State the blood parasite species.
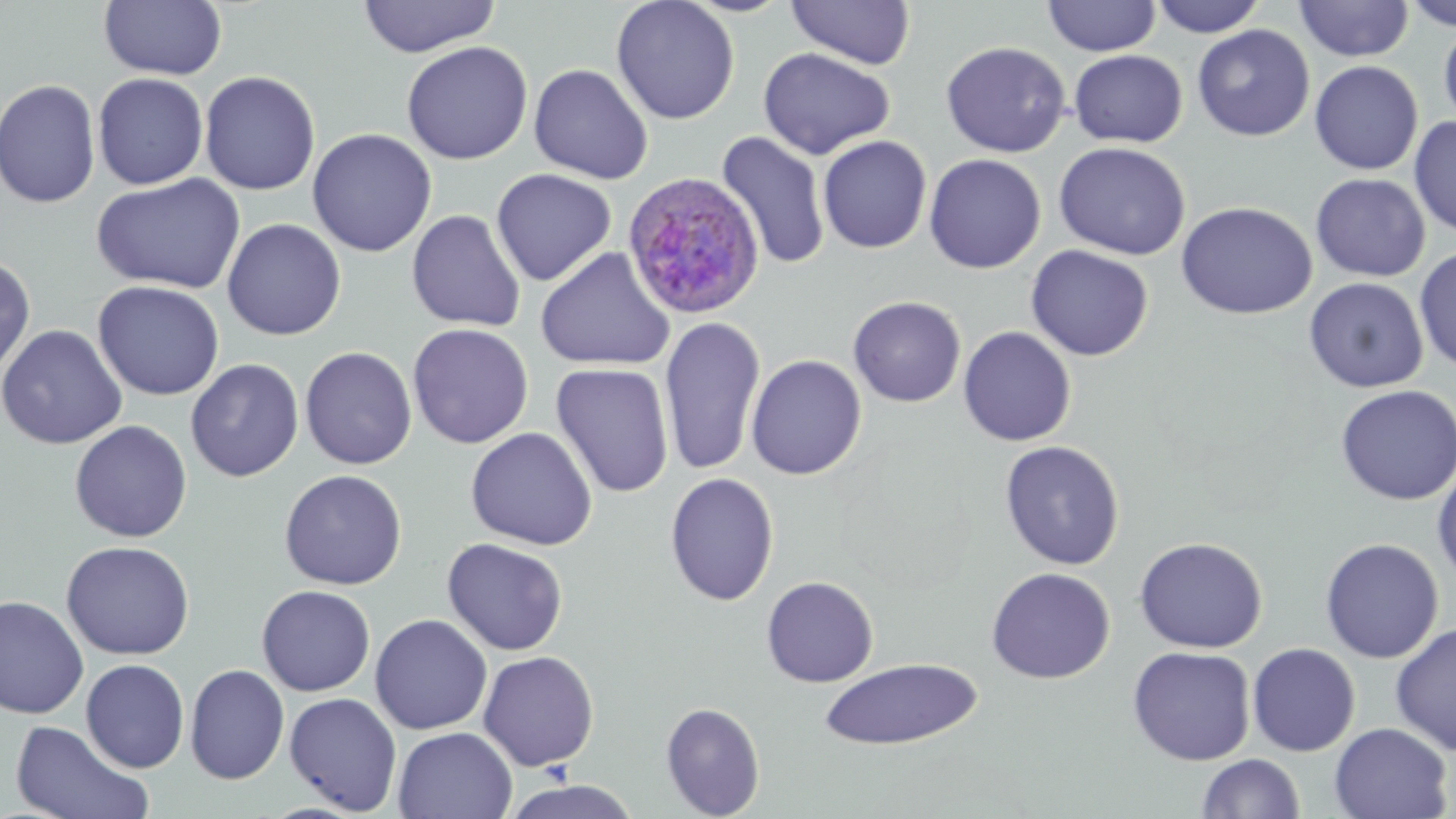
Plasmodium ovale.

Summary:
  - Coordinate format: approximate bounding boxes as (x1, y1, x2, y2) in pixels
  - Plasmodium ovale-infected red blood cell locations: (622, 172, 766, 320)
  - Uninfected red blood cell locations: (99, 0, 227, 80), (358, 0, 500, 57), (611, 0, 740, 125), (787, 0, 916, 69), (1043, 0, 1161, 57), (1150, 0, 1267, 37), (1402, 0, 1456, 31), (1294, 1, 1413, 62), (1439, 18, 1456, 129), (1193, 24, 1315, 141), (401, 41, 533, 164), (940, 41, 1070, 158), (758, 47, 895, 160), (1069, 49, 1188, 148), (1309, 60, 1423, 175), (528, 63, 653, 184), (199, 70, 321, 196), (93, 73, 209, 190), (0, 78, 101, 209), (1409, 116, 1456, 238), (307, 128, 437, 257), (716, 132, 831, 270), (818, 135, 932, 254), (1054, 141, 1191, 261), (923, 151, 1187, 269), (924, 154, 1046, 274), (491, 169, 616, 287), (91, 172, 246, 294), (1311, 173, 1430, 281), (1176, 201, 1317, 320), (407, 209, 526, 332), (222, 218, 346, 341), (1025, 244, 1154, 361), (1414, 246, 1456, 373), (535, 247, 675, 371), (0, 253, 36, 378), (1304, 277, 1428, 393), (92, 280, 225, 401), (848, 296, 966, 407), (659, 317, 765, 477), (407, 323, 534, 449), (0, 324, 127, 449), (958, 326, 1076, 446), (300, 346, 417, 469), (746, 354, 867, 480), (185, 359, 304, 482), (551, 363, 674, 498), (1335, 385, 1456, 505), (69, 420, 192, 543), (465, 427, 598, 551), (999, 440, 1125, 570), (1432, 460, 1456, 585), (278, 469, 407, 590), (664, 472, 780, 607), (1134, 536, 1268, 653), (1320, 537, 1444, 663), (442, 538, 569, 656), (60, 540, 195, 661), (985, 567, 1116, 684), (761, 576, 879, 687), (256, 584, 376, 696), (0, 594, 89, 719), (370, 614, 492, 734), (1391, 623, 1456, 756), (1247, 643, 1361, 756), (1127, 645, 1256, 765), (478, 650, 600, 772), (818, 658, 982, 750), (80, 659, 190, 773), (184, 664, 289, 784), (284, 692, 402, 814), (660, 701, 766, 819), (9, 720, 155, 819), (1329, 722, 1453, 819), (393, 726, 518, 819), (1197, 753, 1305, 818), (497, 779, 646, 819)
  - Field of view: single
  - Image size: 1456×819 pixels
  - Modality: light microscopy
  - Magnification: 1000x
  - Preparation: thin blood film
  - Stain: May-Grünwald-Giemsa